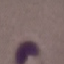

Summary:
  - Malaria status: uninfected
  - Image type: automatically extracted cell patch, resized to 64 × 64 pixels
  - Preparation: thin blood film
  - Stain: Giemsa
  - Capture: smartphone through the microscope eyepiece